Classify this cell by malaria status.
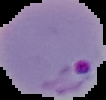
Parasitized.

Summary:
  - Preparation: thin blood film
  - Image type: cell region segmented out of the field of view; surrounding area masked to black
  - Image size: 106×100 pixels